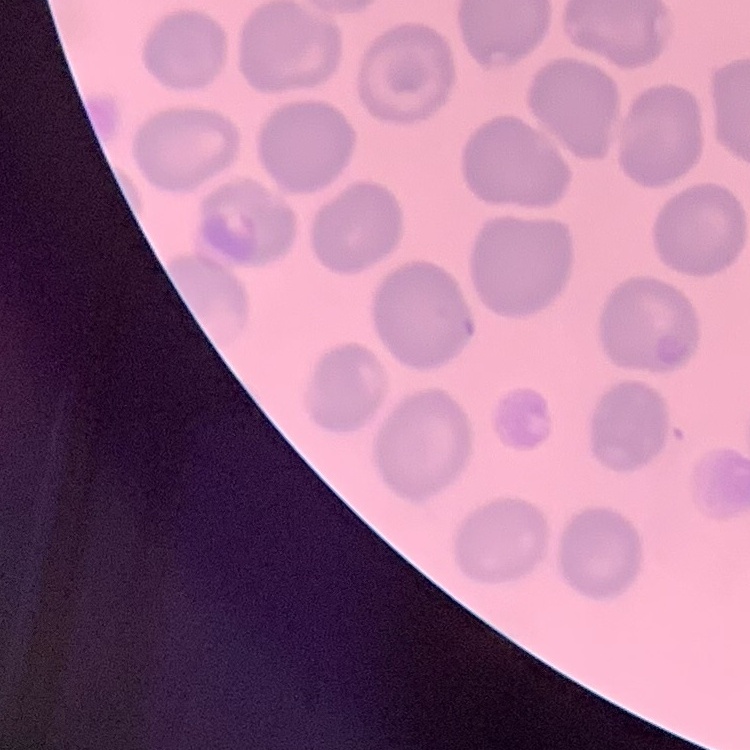

Summary:
  - Erythrocyte morphology: no rouleaux formation
  - Preparation: thin peripheral smear
  - Stain: Field's or Giemsa
  - Image type: square crop of a larger photomicrograph